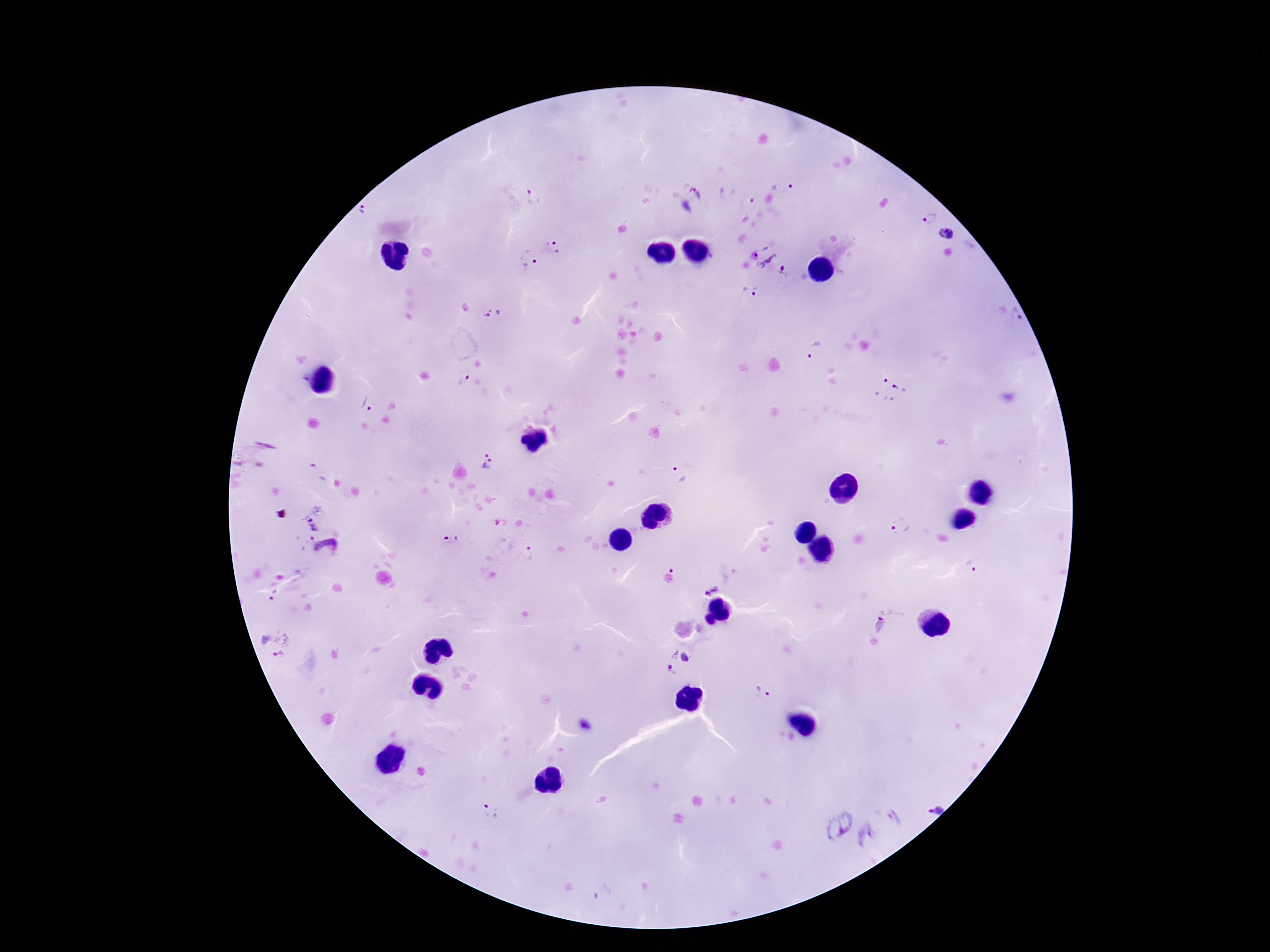
{
  "magnification": "100x",
  "plasmodium_parasite_locations": "approximate centers as (x, y) in pixels: (782, 188), (533, 197), (694, 200), (749, 204), (362, 209), (928, 218), (945, 234), (555, 246), (763, 254), (529, 259), (785, 272), (750, 291), (493, 314), (1016, 314), (814, 351), (464, 378), (890, 389), (365, 404), (492, 461), (680, 477), (312, 516), (899, 526), (451, 541), (325, 550), (526, 553), (973, 564), (710, 586), (274, 595), (879, 625), (275, 645), (679, 661), (763, 691), (937, 808), (491, 811), (835, 821), (868, 836), (602, 892)",
  "preparation": "thick peripheral-blood smear",
  "field_of_view": "single",
  "image_size": "1270×952 pixels",
  "stain": "Giemsa",
  "patient_malaria_status": "infected",
  "capture": "smartphone camera through the microscope eyepiece"
}